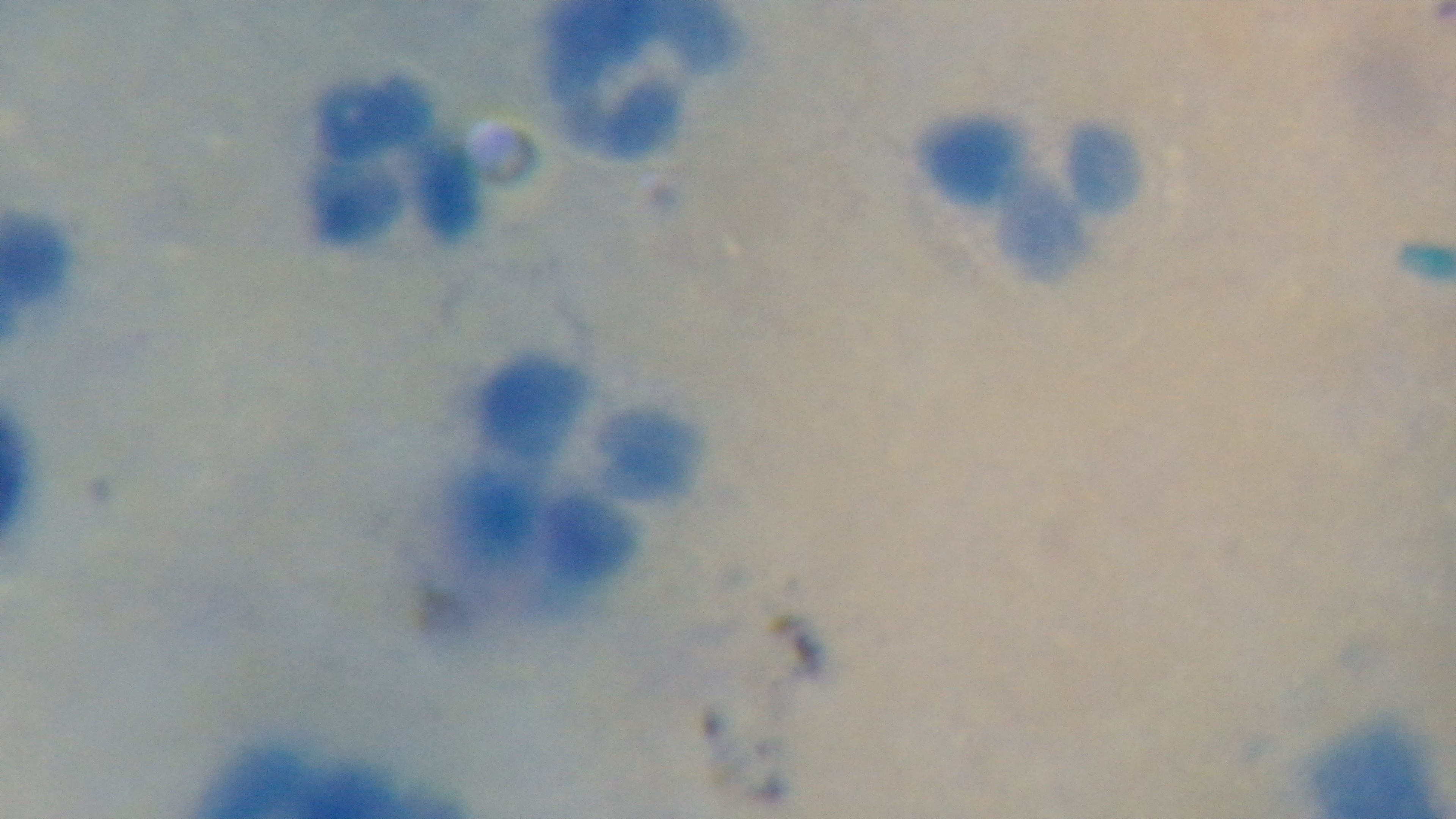

field of view = single
objective = 100x oil immersion
capture = mounted 4K digital camera
stain = Giemsa
malaria status = negative
modality = light microscopy
preparation = thick smear